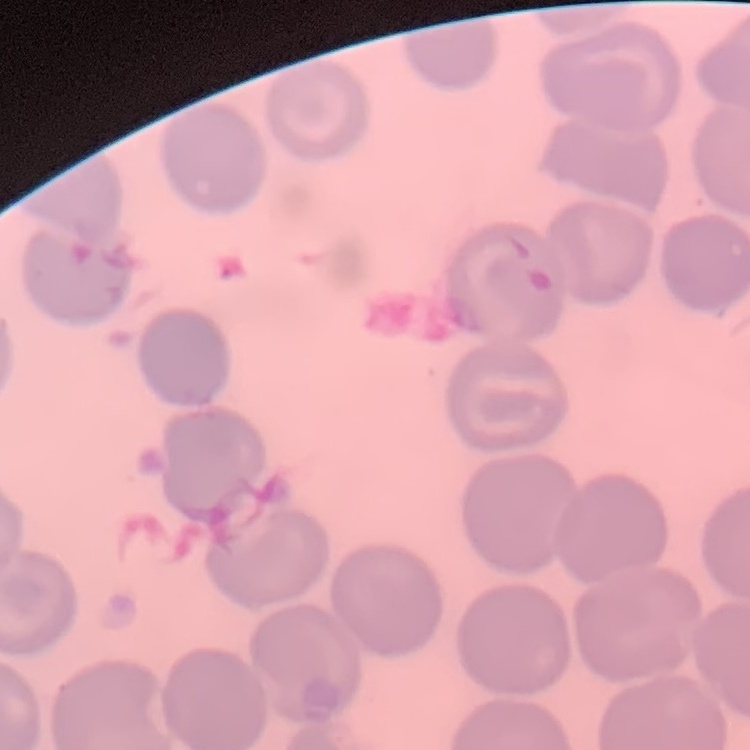
red blood cell morphology = no rouleaux formation
image type = one tile cut from a larger photomicrograph
preparation = thin blood film
stain = Field's or Giemsa